State which parasite is depicted.
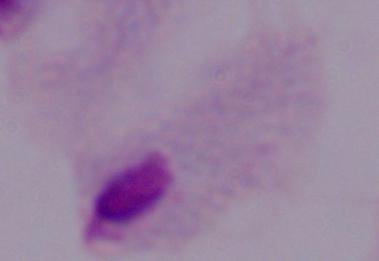

A trichomonad.

Summary:
  - Magnification: 1000x
  - Modality: micrograph